Report the malaria status of this cell.
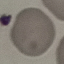
It is uninfected.

Automatically extracted cell patch, resized to 64 × 64 pixels. Acquired by smartphone through the microscope eyepiece. Giemsa stain. Thin blood smear.